Assess this cell for malaria.
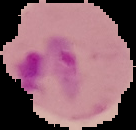

It is parasitized.

{
  "image_type": "cell region segmented out of the field of view; surrounding area masked to black",
  "preparation": "thin blood film",
  "image_size": "136×130 pixels"
}